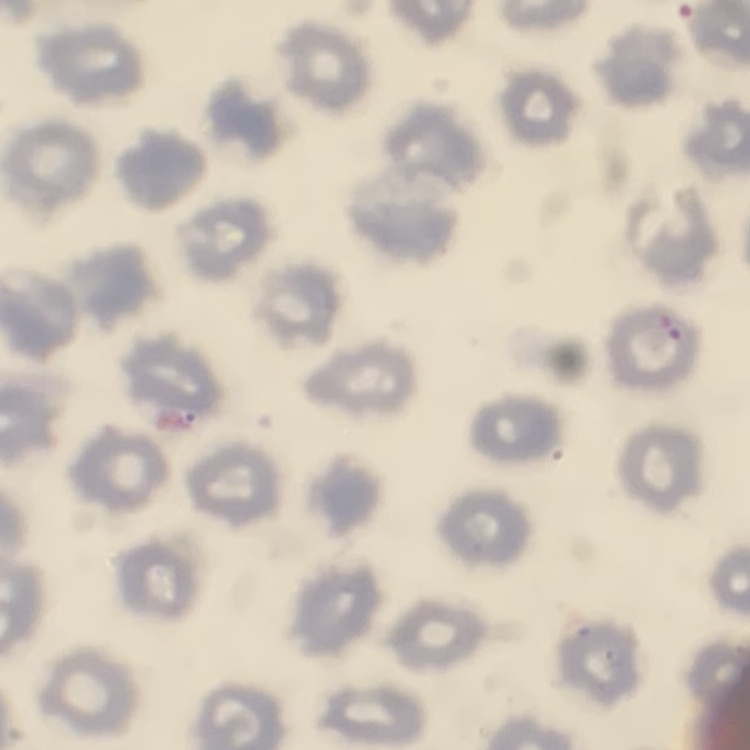
Summary:
  - Erythrocyte morphology: no rouleaux formation
  - Preparation: thin blood smear
  - Image type: one tile cut from a larger photomicrograph
  - Stain: Field's or Giemsa